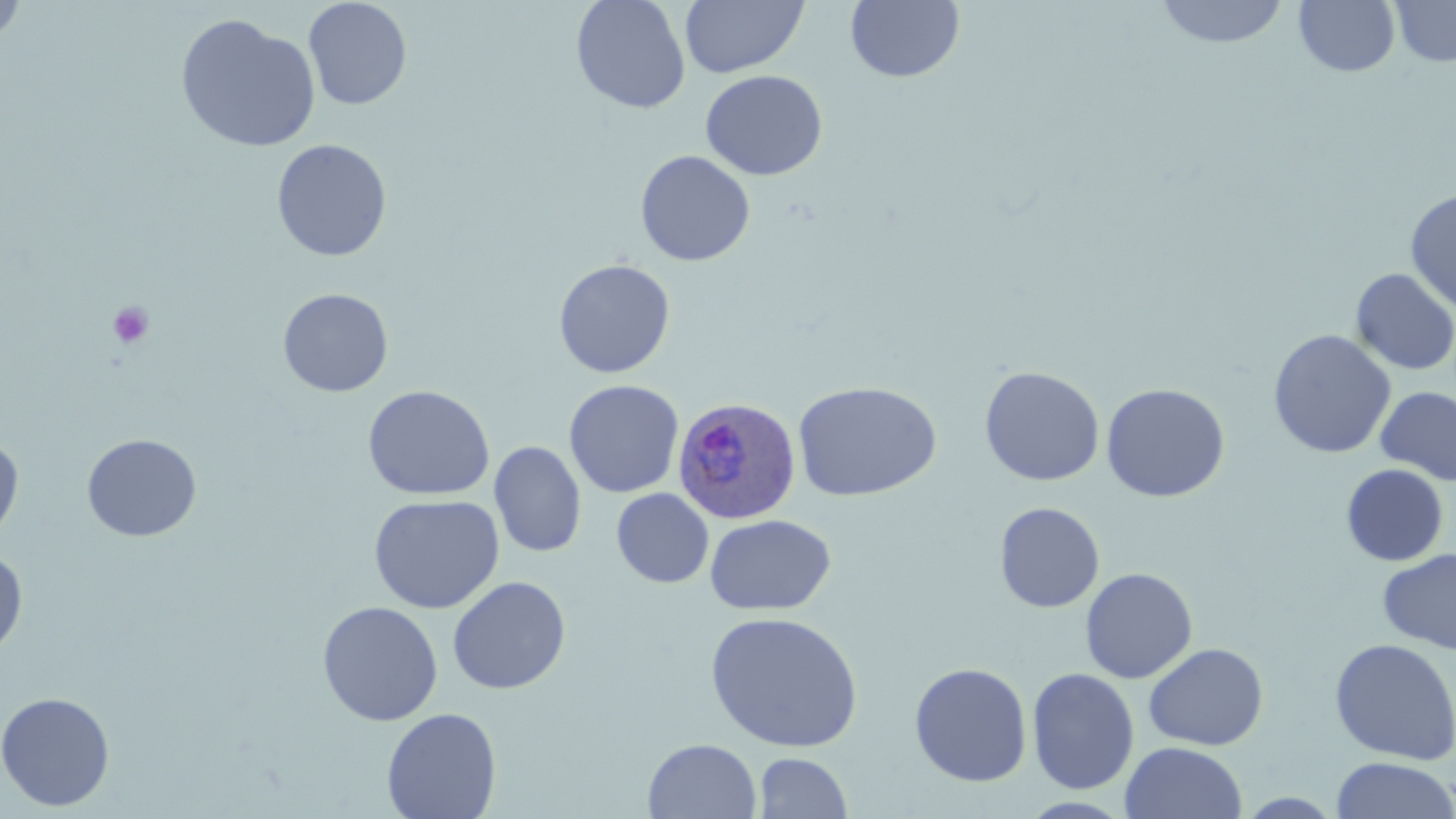

slide-level diagnosis = Plasmodium ovale
stain = May-Grünwald-Giemsa
magnification = 1000x
modality = light microscopy
preparation = thin blood smear
Plasmodium ovale-infected red blood cell locations = approximate bounding boxes as named x1/y1/x2/y2 corners in pixels: (x1=672, y1=395, x2=802, y2=524)
platelet locations = approximate bounding boxes as named x1/y1/x2/y2 corners in pixels: (x1=107, y1=301, x2=154, y2=349)
field of view = one of a larger specimen
image size = 1456×819 pixels
uninfected red blood cell locations = approximate bounding boxes as named x1/y1/x2/y2 corners in pixels: (x1=303, y1=0, x2=413, y2=110), (x1=571, y1=0, x2=691, y2=114), (x1=1153, y1=0, x2=1291, y2=49), (x1=1294, y1=0, x2=1400, y2=77), (x1=0, y1=1, x2=28, y2=47), (x1=680, y1=1, x2=809, y2=78), (x1=846, y1=1, x2=965, y2=83), (x1=1389, y1=1, x2=1456, y2=67), (x1=175, y1=13, x2=322, y2=153), (x1=700, y1=70, x2=828, y2=180), (x1=271, y1=139, x2=392, y2=262), (x1=635, y1=150, x2=755, y2=266), (x1=1404, y1=187, x2=1456, y2=315), (x1=553, y1=259, x2=676, y2=378), (x1=1350, y1=268, x2=1456, y2=375), (x1=277, y1=287, x2=394, y2=397), (x1=1268, y1=329, x2=1396, y2=459), (x1=979, y1=366, x2=1105, y2=486), (x1=564, y1=380, x2=684, y2=498), (x1=792, y1=381, x2=943, y2=502), (x1=1100, y1=383, x2=1230, y2=503), (x1=362, y1=385, x2=495, y2=501), (x1=1375, y1=386, x2=1456, y2=487), (x1=0, y1=432, x2=24, y2=544), (x1=82, y1=433, x2=202, y2=542), (x1=489, y1=441, x2=586, y2=557), (x1=1340, y1=464, x2=1448, y2=566), (x1=611, y1=489, x2=713, y2=588), (x1=368, y1=494, x2=505, y2=613), (x1=994, y1=502, x2=1105, y2=613), (x1=705, y1=514, x2=836, y2=616), (x1=0, y1=547, x2=28, y2=660), (x1=1377, y1=547, x2=1456, y2=655), (x1=1080, y1=567, x2=1198, y2=683), (x1=447, y1=576, x2=571, y2=695), (x1=317, y1=601, x2=443, y2=726), (x1=704, y1=611, x2=864, y2=752), (x1=1329, y1=638, x2=1456, y2=765), (x1=1143, y1=643, x2=1269, y2=750), (x1=909, y1=661, x2=1033, y2=787), (x1=1026, y1=667, x2=1140, y2=795), (x1=0, y1=691, x2=116, y2=812), (x1=381, y1=707, x2=502, y2=819), (x1=643, y1=738, x2=762, y2=819), (x1=1120, y1=741, x2=1248, y2=819), (x1=753, y1=752, x2=852, y2=818), (x1=1330, y1=756, x2=1456, y2=819)